State the blood parasite species.
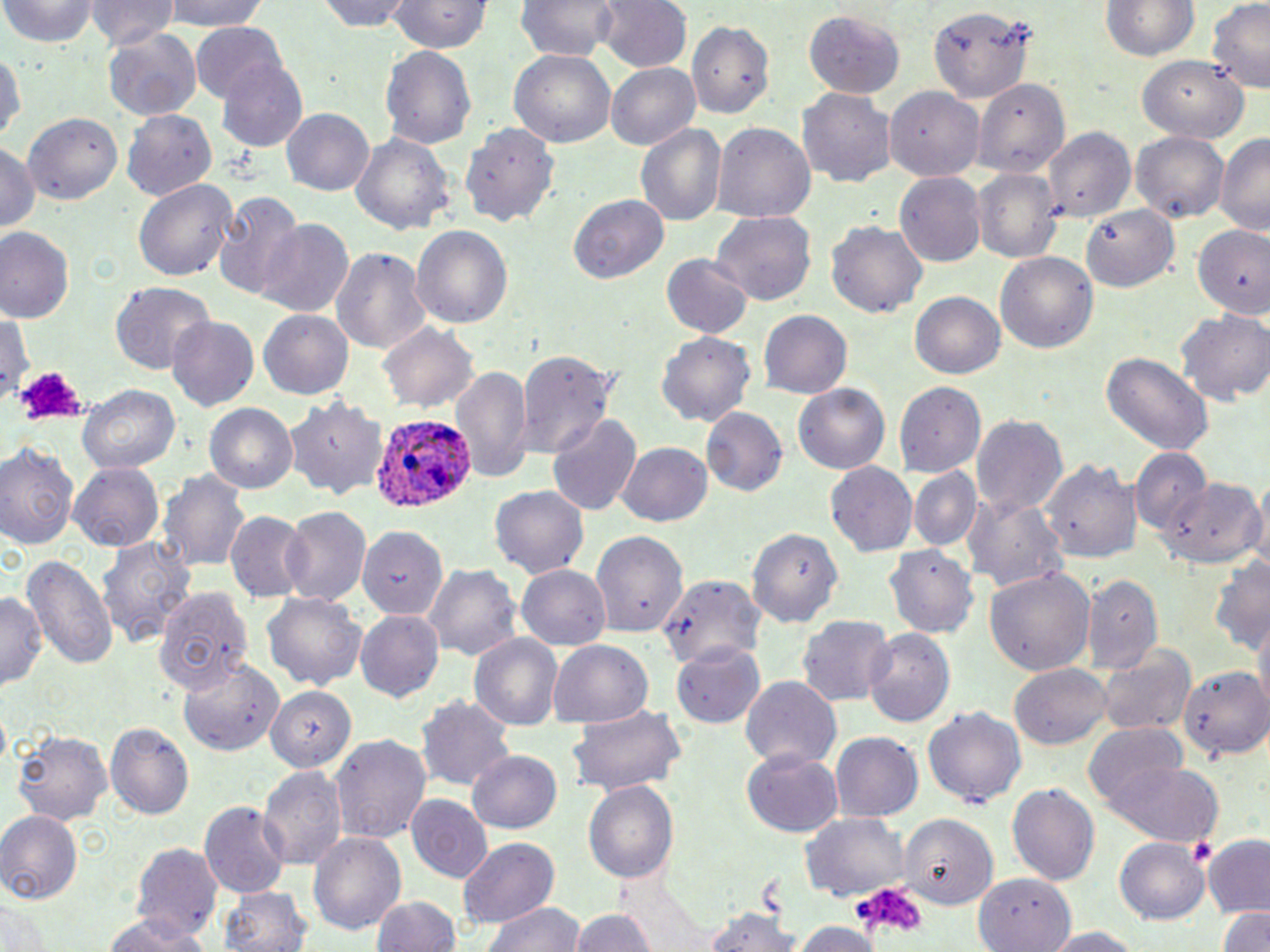
Plasmodium ovale.

Approximate bounding boxes as named x1/y1/x2/y2 corners in pixels. Uninfected red blood cell locations: (x1=2, y1=0, x2=99, y2=47), (x1=87, y1=0, x2=177, y2=49), (x1=155, y1=0, x2=278, y2=29), (x1=316, y1=0, x2=418, y2=31), (x1=389, y1=0, x2=491, y2=56), (x1=598, y1=0, x2=689, y2=72), (x1=1100, y1=0, x2=1201, y2=62), (x1=518, y1=1, x2=619, y2=61), (x1=929, y1=2, x2=1034, y2=110), (x1=1209, y1=2, x2=1270, y2=92), (x1=95, y1=4, x2=186, y2=92), (x1=800, y1=10, x2=903, y2=100), (x1=690, y1=21, x2=776, y2=119), (x1=191, y1=23, x2=288, y2=106), (x1=104, y1=30, x2=200, y2=119), (x1=0, y1=41, x2=25, y2=148), (x1=382, y1=46, x2=477, y2=151), (x1=510, y1=50, x2=616, y2=147), (x1=1136, y1=55, x2=1253, y2=142), (x1=216, y1=56, x2=309, y2=154), (x1=606, y1=62, x2=700, y2=149), (x1=976, y1=77, x2=1071, y2=175), (x1=886, y1=87, x2=985, y2=179), (x1=799, y1=88, x2=896, y2=190), (x1=18, y1=105, x2=124, y2=208), (x1=122, y1=107, x2=215, y2=199), (x1=282, y1=108, x2=373, y2=194), (x1=458, y1=119, x2=566, y2=228), (x1=713, y1=123, x2=815, y2=222), (x1=635, y1=126, x2=725, y2=225), (x1=1045, y1=128, x2=1134, y2=222), (x1=1132, y1=129, x2=1230, y2=224), (x1=352, y1=132, x2=454, y2=239), (x1=1214, y1=132, x2=1270, y2=236), (x1=0, y1=141, x2=40, y2=240), (x1=975, y1=167, x2=1061, y2=264), (x1=897, y1=173, x2=986, y2=268), (x1=135, y1=178, x2=238, y2=283), (x1=214, y1=191, x2=304, y2=300), (x1=570, y1=197, x2=668, y2=283), (x1=1082, y1=205, x2=1181, y2=292), (x1=712, y1=211, x2=817, y2=307), (x1=1189, y1=219, x2=1270, y2=320), (x1=255, y1=220, x2=354, y2=317), (x1=828, y1=223, x2=927, y2=317), (x1=411, y1=225, x2=513, y2=331), (x1=0, y1=226, x2=76, y2=325), (x1=329, y1=246, x2=432, y2=355), (x1=995, y1=251, x2=1098, y2=354), (x1=661, y1=255, x2=753, y2=341), (x1=109, y1=281, x2=215, y2=375), (x1=910, y1=290, x2=1007, y2=378), (x1=259, y1=309, x2=354, y2=400), (x1=1177, y1=309, x2=1270, y2=404), (x1=759, y1=311, x2=852, y2=397), (x1=1, y1=312, x2=31, y2=404), (x1=166, y1=315, x2=259, y2=412), (x1=378, y1=323, x2=480, y2=413), (x1=656, y1=331, x2=755, y2=426), (x1=515, y1=349, x2=619, y2=457), (x1=1101, y1=353, x2=1214, y2=455), (x1=452, y1=365, x2=532, y2=482), (x1=896, y1=383, x2=986, y2=477), (x1=76, y1=384, x2=181, y2=473), (x1=793, y1=385, x2=888, y2=473), (x1=286, y1=396, x2=389, y2=501), (x1=204, y1=402, x2=298, y2=495), (x1=702, y1=409, x2=787, y2=497), (x1=547, y1=414, x2=640, y2=515), (x1=971, y1=414, x2=1068, y2=521), (x1=617, y1=442, x2=714, y2=526), (x1=0, y1=443, x2=80, y2=551), (x1=1130, y1=447, x2=1209, y2=536), (x1=1044, y1=460, x2=1141, y2=565), (x1=68, y1=462, x2=166, y2=551), (x1=827, y1=463, x2=917, y2=557), (x1=908, y1=467, x2=981, y2=551), (x1=162, y1=469, x2=250, y2=574), (x1=1159, y1=478, x2=1263, y2=572), (x1=490, y1=484, x2=592, y2=578), (x1=962, y1=493, x2=1067, y2=595), (x1=278, y1=504, x2=369, y2=606), (x1=225, y1=512, x2=308, y2=601), (x1=749, y1=524, x2=845, y2=628), (x1=357, y1=527, x2=449, y2=619), (x1=590, y1=531, x2=689, y2=636), (x1=97, y1=535, x2=198, y2=649), (x1=883, y1=544, x2=976, y2=638), (x1=23, y1=551, x2=118, y2=675), (x1=1211, y1=553, x2=1268, y2=655), (x1=422, y1=562, x2=522, y2=660), (x1=517, y1=564, x2=612, y2=651), (x1=985, y1=565, x2=1095, y2=674), (x1=660, y1=571, x2=767, y2=671), (x1=1081, y1=576, x2=1161, y2=676), (x1=156, y1=586, x2=255, y2=697), (x1=263, y1=591, x2=366, y2=693), (x1=0, y1=592, x2=45, y2=690), (x1=355, y1=611, x2=443, y2=701), (x1=798, y1=614, x2=893, y2=703), (x1=864, y1=628, x2=955, y2=728), (x1=470, y1=633, x2=563, y2=731), (x1=548, y1=640, x2=651, y2=725), (x1=673, y1=641, x2=768, y2=727), (x1=1100, y1=643, x2=1195, y2=738), (x1=177, y1=658, x2=280, y2=757), (x1=1012, y1=664, x2=1113, y2=749), (x1=1181, y1=665, x2=1270, y2=759), (x1=738, y1=675, x2=841, y2=771), (x1=266, y1=684, x2=355, y2=771), (x1=419, y1=697, x2=514, y2=789), (x1=564, y1=705, x2=688, y2=795), (x1=923, y1=706, x2=1025, y2=808), (x1=105, y1=723, x2=194, y2=821), (x1=1085, y1=725, x2=1188, y2=816), (x1=10, y1=731, x2=114, y2=823), (x1=330, y1=733, x2=432, y2=844), (x1=831, y1=733, x2=924, y2=823), (x1=467, y1=748, x2=562, y2=834), (x1=740, y1=751, x2=844, y2=838), (x1=1101, y1=760, x2=1222, y2=845), (x1=257, y1=763, x2=346, y2=872), (x1=582, y1=781, x2=679, y2=887), (x1=1008, y1=782, x2=1101, y2=890), (x1=407, y1=797, x2=495, y2=883), (x1=200, y1=801, x2=290, y2=895), (x1=0, y1=809, x2=82, y2=905), (x1=899, y1=811, x2=999, y2=906), (x1=800, y1=812, x2=908, y2=900), (x1=309, y1=832, x2=406, y2=937), (x1=1198, y1=835, x2=1270, y2=916), (x1=456, y1=836, x2=559, y2=928), (x1=1117, y1=836, x2=1212, y2=923), (x1=132, y1=842, x2=223, y2=942), (x1=975, y1=875, x2=1074, y2=952), (x1=220, y1=884, x2=310, y2=952), (x1=369, y1=894, x2=465, y2=951), (x1=1, y1=900, x2=52, y2=950), (x1=485, y1=901, x2=584, y2=952), (x1=1216, y1=905, x2=1270, y2=952), (x1=565, y1=908, x2=661, y2=952), (x1=704, y1=908, x2=802, y2=952), (x1=100, y1=915, x2=208, y2=952), (x1=792, y1=919, x2=883, y2=951), (x1=1035, y1=926, x2=1146, y2=950). Plasmodium ovale-infected red blood cell locations: (x1=365, y1=412, x2=475, y2=515). Platelet locations: (x1=13, y1=366, x2=88, y2=427), (x1=1185, y1=836, x2=1218, y2=863), (x1=854, y1=883, x2=926, y2=938). Thin blood smear. May-Grünwald-Giemsa-stained preparation. One field of a larger specimen. Image is 1270×952 pixels. Light microscopy. 1000x magnification.